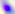

magnification = 400x
identification = Toxoplasma gondii
modality = photomicrograph